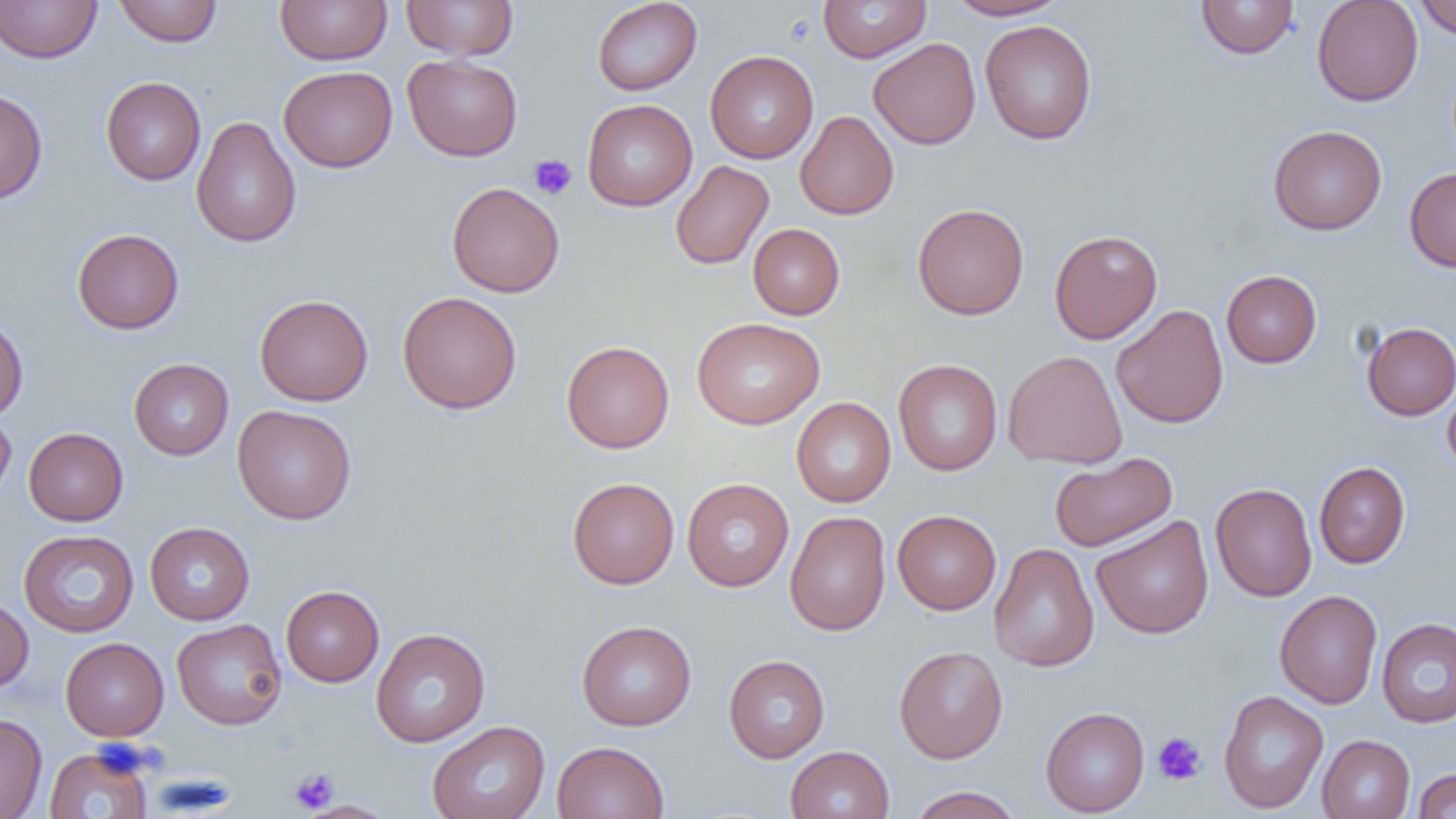 Approximate bounding boxes as (x1, y1, x2, y2) in pixels. Uninfected red blood cell locations: (0, 0, 102, 63), (113, 0, 223, 46), (275, 0, 392, 65), (401, 0, 518, 60), (592, 0, 702, 95), (818, 0, 931, 63), (945, 0, 1068, 20), (1195, 0, 1300, 59), (1312, 0, 1423, 106), (1413, 0, 1456, 40), (980, 19, 1098, 144), (868, 37, 981, 150), (705, 50, 818, 163), (403, 54, 522, 161), (279, 66, 397, 172), (101, 77, 206, 185), (0, 87, 48, 205), (582, 99, 697, 211), (795, 111, 899, 220), (190, 116, 302, 248), (1268, 124, 1387, 235), (670, 160, 774, 270), (1404, 168, 1456, 272), (446, 182, 565, 298), (913, 204, 1029, 320), (748, 223, 845, 319), (72, 228, 184, 333), (1049, 229, 1162, 344), (1221, 270, 1322, 368), (397, 291, 522, 414), (255, 294, 373, 406), (1111, 305, 1228, 428), (0, 316, 29, 421), (692, 317, 825, 429), (1361, 322, 1456, 420), (561, 340, 674, 453), (1003, 350, 1127, 469), (129, 358, 233, 460), (893, 359, 1002, 476), (1442, 382, 1456, 476), (791, 397, 896, 507), (232, 405, 357, 524), (0, 410, 17, 503), (24, 427, 128, 526), (1049, 453, 1176, 551), (1314, 461, 1411, 569), (567, 477, 679, 589), (681, 478, 794, 591), (1210, 483, 1317, 602), (892, 510, 1001, 614), (785, 511, 891, 636), (1091, 515, 1214, 640), (145, 522, 255, 624), (18, 530, 139, 637), (988, 542, 1099, 673), (281, 585, 384, 687), (1274, 590, 1383, 708), (0, 596, 34, 693), (1376, 617, 1456, 728), (171, 619, 287, 730), (577, 620, 696, 731), (370, 628, 490, 747), (60, 637, 169, 741), (894, 645, 1008, 763), (723, 655, 830, 763), (1218, 690, 1328, 813), (1040, 707, 1150, 816), (0, 713, 47, 819), (427, 721, 549, 819), (1317, 734, 1415, 819), (552, 741, 669, 819), (44, 745, 154, 818), (786, 745, 895, 819), (1412, 768, 1456, 818), (908, 786, 1023, 819). Platelet locations: (529, 154, 577, 200), (1153, 732, 1206, 786), (290, 768, 340, 813). Slide-level diagnosis: no evidence of blood parasites. Thin blood smear. Captured at 1000x magnification. Single field of view. Image is 1456×819 pixels. Light microscopy.